Identify the preparation type.
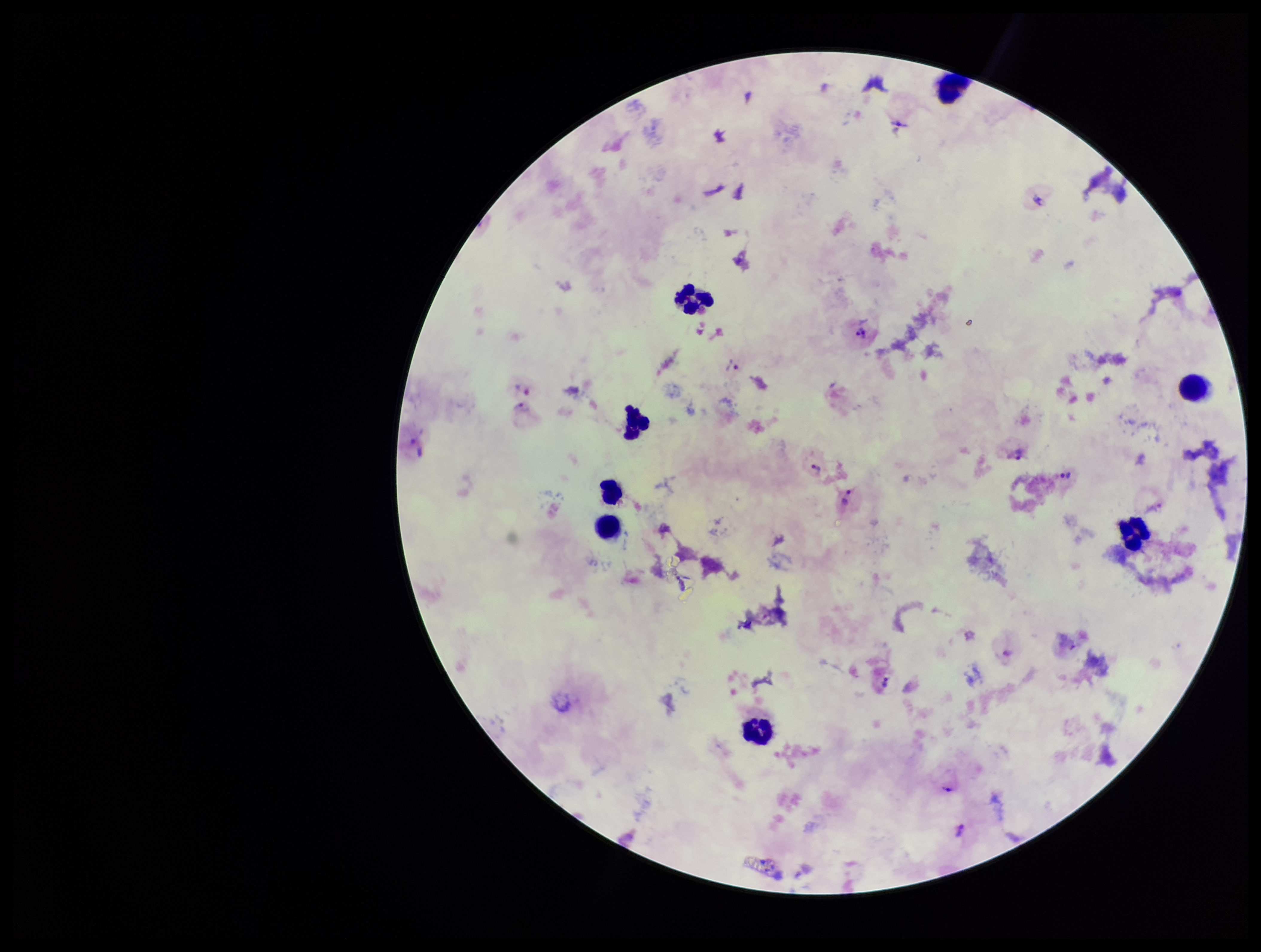

A thick smear.

Parasite count: 11. Smartphone photograph taken through the eyepiece of a microscope. Stained with Giemsa. Leukocyte count: 8. Plasmodium parasites: seen. One field from this slide. Patient malaria status: positive. Image is 1261×952 pixels. Species reported for this patient: Plasmodium vivax.